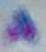 Toxoplasma gondii is shown. 1000x magnification. Photomicrograph.